Evaluate for malaria.
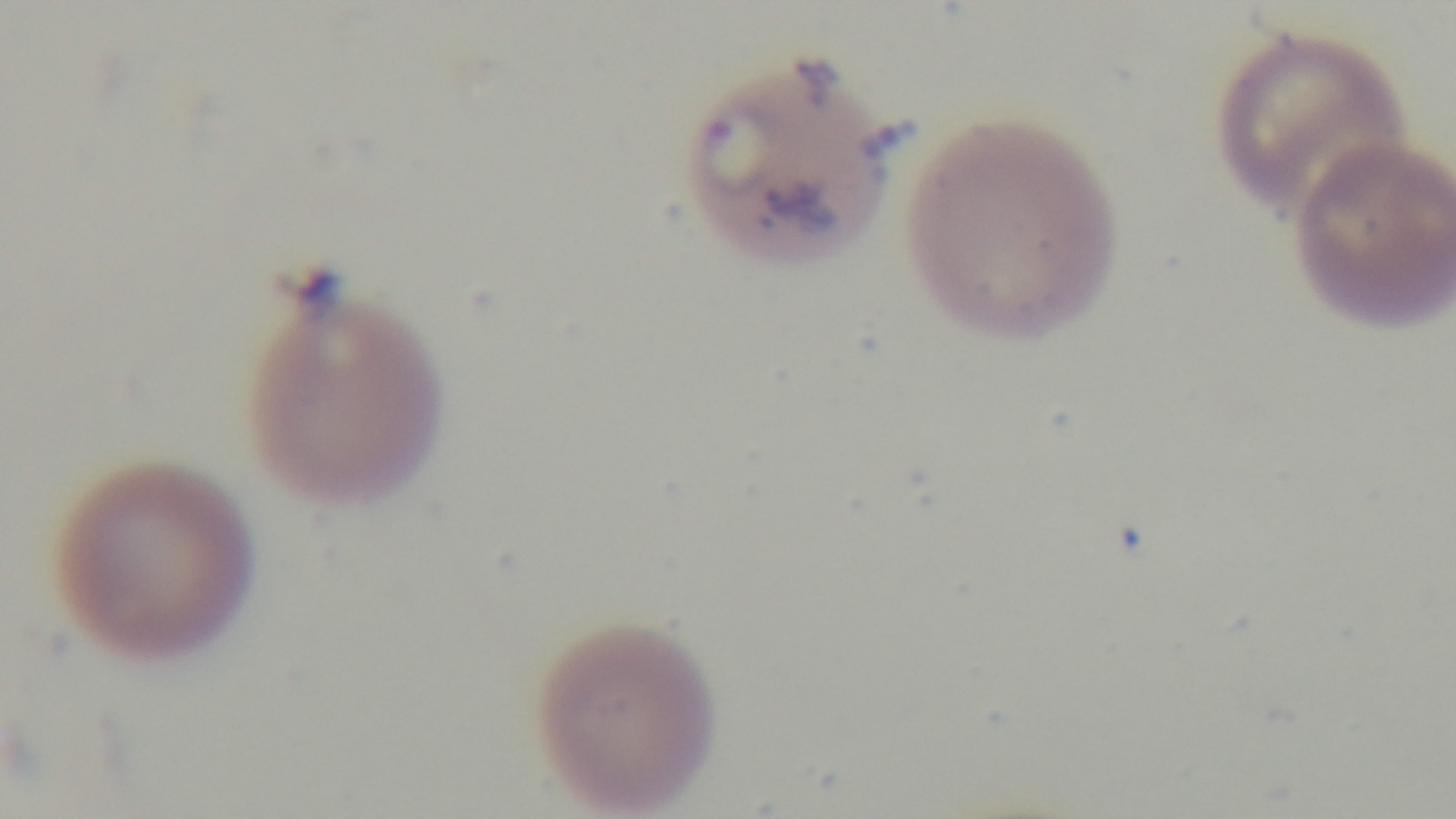
Infected.

Single field of view. Giemsa-stained. Photomicrograph. Oil-immersion objective, 100x. Preparation: thin blood film. Captured with a mounted 4K digital camera.